Describe the morphology of the erythrocytes.
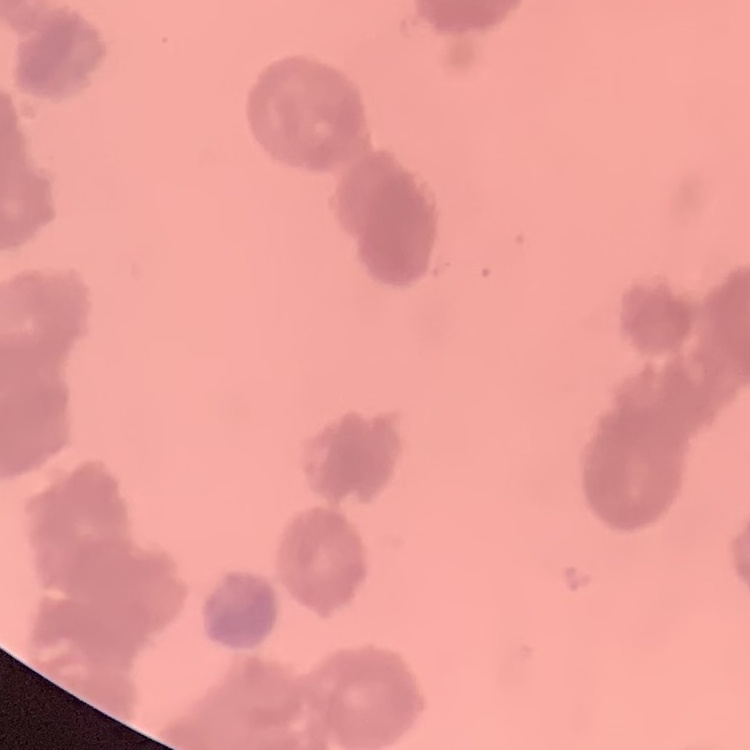
They show rouleaux formation.

Square crop of a larger photomicrograph. Field's or Giemsa stain. Thin blood film.